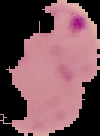

malaria status = parasitized
preparation = thin blood film
image size = 100×136 pixels
image type = cell region segmented out of the field of view; surrounding area masked to black